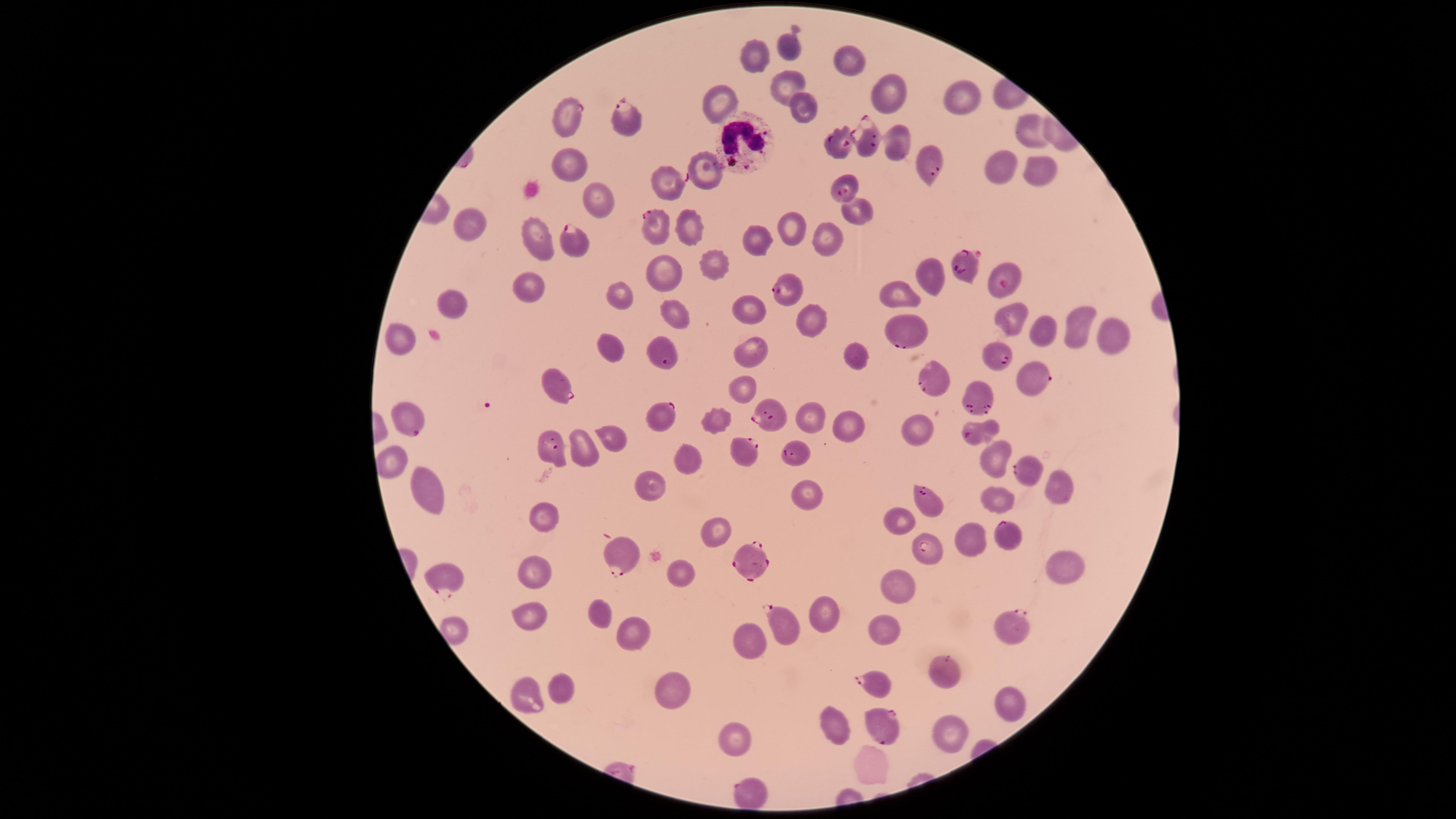

Approximate marker points, in pixels from the top-left corner.
Summary:
  - Uninfected red blood cells: (x=785, y=46), (x=749, y=59), (x=847, y=61), (x=788, y=79), (x=885, y=89), (x=966, y=98), (x=716, y=103), (x=804, y=111), (x=1027, y=130), (x=896, y=145), (x=567, y=163), (x=999, y=164), (x=705, y=168), (x=1024, y=168), (x=588, y=197), (x=857, y=212), (x=796, y=223), (x=471, y=224), (x=693, y=227), (x=830, y=237), (x=749, y=238), (x=535, y=240), (x=713, y=264), (x=929, y=274), (x=665, y=277), (x=529, y=284), (x=620, y=295), (x=906, y=300), (x=453, y=302), (x=750, y=303), (x=673, y=310), (x=807, y=320), (x=1015, y=322), (x=1078, y=322), (x=1045, y=330), (x=1109, y=338), (x=395, y=340), (x=749, y=344), (x=612, y=345), (x=857, y=356), (x=745, y=392), (x=716, y=414), (x=808, y=414), (x=847, y=422), (x=913, y=427), (x=607, y=436), (x=584, y=449), (x=992, y=457), (x=685, y=458), (x=390, y=466), (x=650, y=483), (x=1060, y=483), (x=801, y=490), (x=432, y=494), (x=999, y=497), (x=545, y=507), (x=897, y=517), (x=717, y=529), (x=975, y=534), (x=1062, y=567), (x=535, y=569), (x=678, y=571), (x=894, y=586), (x=531, y=609), (x=823, y=612), (x=598, y=614), (x=884, y=627), (x=632, y=634), (x=749, y=642), (x=673, y=685), (x=562, y=688), (x=523, y=696), (x=1006, y=701), (x=836, y=725), (x=947, y=731), (x=738, y=738), (x=870, y=764)
  - White blood cells: (x=742, y=141)
  - Parasitized red blood cells: (x=566, y=115), (x=626, y=124), (x=870, y=142), (x=839, y=145), (x=925, y=163), (x=663, y=180), (x=843, y=185), (x=657, y=228), (x=573, y=241), (x=960, y=264), (x=1005, y=279), (x=790, y=289), (x=904, y=331), (x=664, y=353), (x=998, y=356), (x=1034, y=377), (x=934, y=381), (x=559, y=387), (x=977, y=398), (x=666, y=414), (x=771, y=415), (x=409, y=418), (x=979, y=431), (x=553, y=446), (x=742, y=450), (x=797, y=452), (x=1031, y=473), (x=926, y=500), (x=1005, y=537), (x=928, y=550), (x=622, y=553), (x=756, y=560), (x=448, y=577), (x=1014, y=627), (x=785, y=628), (x=944, y=667), (x=876, y=683), (x=882, y=726), (x=747, y=786)
  - Capture: smartphone photograph through the microscope eyepiece
  - Image size: 1456×819 pixels
  - Field of view: single
  - Stain: Giemsa
  - Presence: malaria parasites identified
  - Visible region: circular
  - Preparation: thin smear of blood
  - Species: Plasmodium falciparum